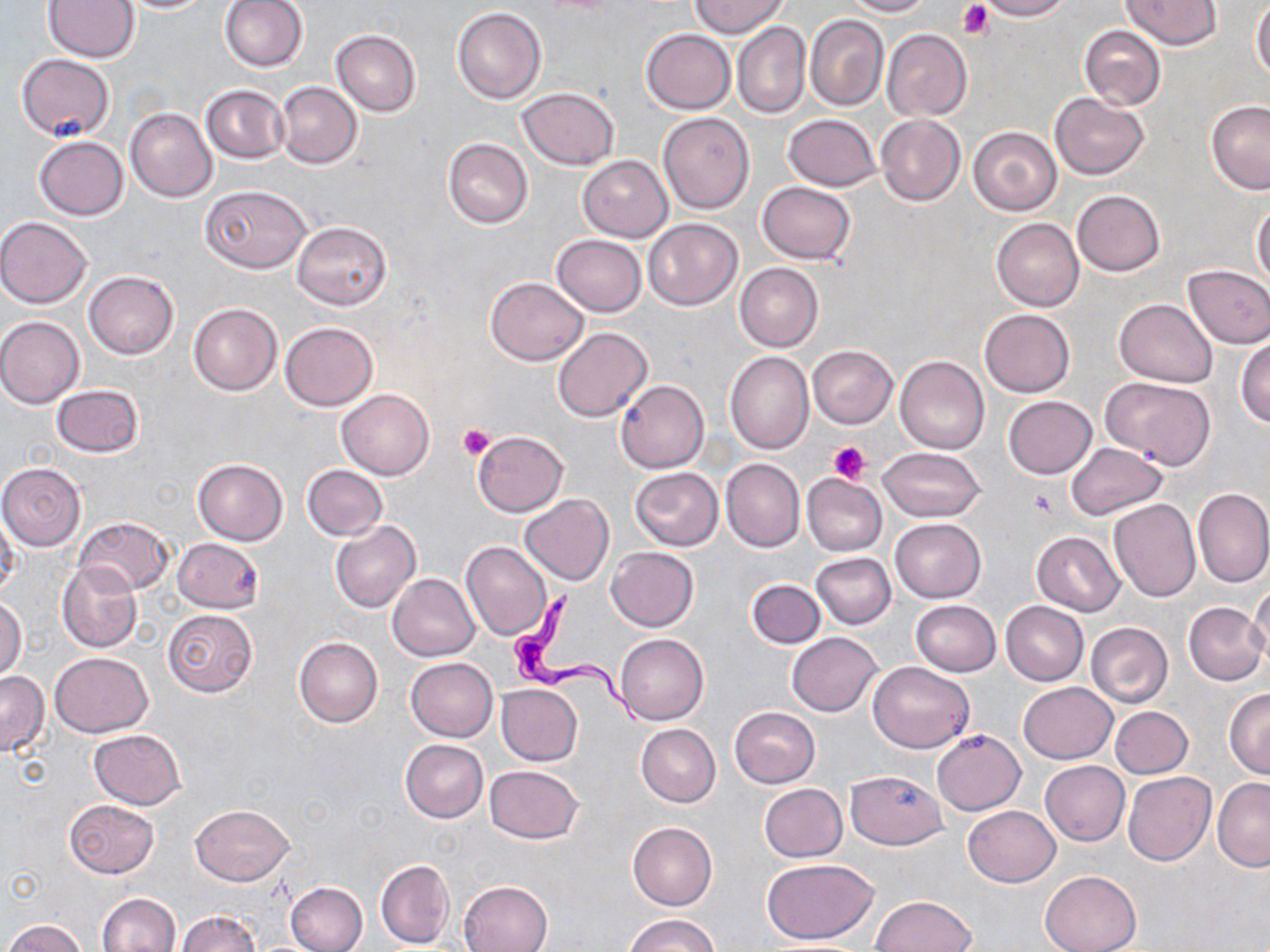

{
  "trypanosoma_brucei_locations": "approximate bounding boxes as named x1/y1/x2/y2 corners in pixels: (x1=506, y1=591, x2=645, y2=728)",
  "slide_level_diagnosis": "Trypanosoma brucei",
  "preparation": "thin blood film",
  "image_size": "1270×952 pixels",
  "platelet_locations": "approximate bounding boxes as named x1/y1/x2/y2 corners in pixels: (x1=958, y1=0, x2=994, y2=39), (x1=457, y1=424, x2=495, y2=459), (x1=829, y1=442, x2=870, y2=484), (x1=1028, y1=487, x2=1059, y2=517)",
  "magnification": "1000x",
  "stain": "May-Grünwald-Giemsa",
  "uninfected_red_blood_cell_locations": "approximate bounding boxes as named x1/y1/x2/y2 corners in pixels: (x1=219, y1=0, x2=308, y2=73), (x1=844, y1=0, x2=933, y2=16), (x1=974, y1=0, x2=1073, y2=21), (x1=1121, y1=0, x2=1219, y2=49), (x1=117, y1=1, x2=216, y2=13), (x1=691, y1=1, x2=785, y2=38), (x1=44, y1=2, x2=138, y2=62), (x1=1251, y1=2, x2=1270, y2=81), (x1=452, y1=7, x2=547, y2=105), (x1=804, y1=15, x2=889, y2=111), (x1=733, y1=22, x2=811, y2=119), (x1=1078, y1=25, x2=1166, y2=110), (x1=641, y1=28, x2=735, y2=114), (x1=330, y1=29, x2=421, y2=116), (x1=882, y1=29, x2=971, y2=120), (x1=18, y1=54, x2=115, y2=140), (x1=275, y1=82, x2=361, y2=168), (x1=201, y1=85, x2=289, y2=162), (x1=517, y1=87, x2=619, y2=170), (x1=1050, y1=92, x2=1149, y2=179), (x1=1206, y1=101, x2=1270, y2=195), (x1=124, y1=108, x2=217, y2=201), (x1=658, y1=112, x2=754, y2=214), (x1=783, y1=114, x2=881, y2=191), (x1=875, y1=114, x2=966, y2=207), (x1=968, y1=126, x2=1061, y2=216), (x1=34, y1=137, x2=129, y2=220), (x1=443, y1=138, x2=532, y2=228), (x1=578, y1=155, x2=673, y2=241), (x1=758, y1=181, x2=855, y2=263), (x1=200, y1=184, x2=311, y2=273), (x1=1072, y1=190, x2=1164, y2=276), (x1=1251, y1=201, x2=1270, y2=284), (x1=0, y1=217, x2=91, y2=308), (x1=644, y1=218, x2=742, y2=310), (x1=991, y1=218, x2=1084, y2=311), (x1=292, y1=221, x2=393, y2=310), (x1=550, y1=234, x2=646, y2=316), (x1=735, y1=263, x2=824, y2=351), (x1=1182, y1=263, x2=1270, y2=349), (x1=85, y1=271, x2=179, y2=358), (x1=484, y1=276, x2=589, y2=365), (x1=1115, y1=298, x2=1217, y2=387), (x1=188, y1=303, x2=281, y2=395), (x1=979, y1=309, x2=1075, y2=397), (x1=0, y1=316, x2=85, y2=408), (x1=279, y1=322, x2=378, y2=411), (x1=552, y1=328, x2=652, y2=422), (x1=1235, y1=338, x2=1270, y2=430), (x1=808, y1=345, x2=897, y2=428), (x1=725, y1=352, x2=813, y2=453), (x1=895, y1=356, x2=989, y2=454), (x1=1101, y1=376, x2=1216, y2=468), (x1=616, y1=379, x2=710, y2=473), (x1=51, y1=384, x2=144, y2=457), (x1=337, y1=389, x2=434, y2=480), (x1=1003, y1=396, x2=1096, y2=479), (x1=472, y1=431, x2=568, y2=516), (x1=1066, y1=442, x2=1168, y2=520), (x1=877, y1=447, x2=985, y2=523), (x1=721, y1=458, x2=805, y2=551), (x1=193, y1=459, x2=289, y2=545), (x1=0, y1=464, x2=87, y2=549), (x1=301, y1=465, x2=388, y2=541), (x1=629, y1=467, x2=724, y2=551), (x1=803, y1=472, x2=888, y2=557), (x1=1192, y1=488, x2=1270, y2=588), (x1=520, y1=495, x2=614, y2=585), (x1=1108, y1=500, x2=1201, y2=602), (x1=1, y1=510, x2=19, y2=599), (x1=75, y1=516, x2=175, y2=596), (x1=889, y1=518, x2=986, y2=602), (x1=330, y1=520, x2=421, y2=613), (x1=1031, y1=531, x2=1124, y2=617), (x1=171, y1=538, x2=264, y2=611), (x1=461, y1=541, x2=553, y2=641), (x1=606, y1=548, x2=698, y2=631), (x1=810, y1=553, x2=896, y2=629), (x1=57, y1=561, x2=141, y2=654), (x1=386, y1=573, x2=479, y2=661), (x1=746, y1=579, x2=826, y2=648), (x1=1248, y1=582, x2=1270, y2=666), (x1=0, y1=597, x2=25, y2=682), (x1=910, y1=600, x2=1001, y2=677), (x1=1000, y1=601, x2=1088, y2=685), (x1=1183, y1=601, x2=1267, y2=685), (x1=163, y1=609, x2=257, y2=697), (x1=1085, y1=622, x2=1173, y2=707), (x1=786, y1=631, x2=881, y2=717), (x1=615, y1=634, x2=709, y2=725), (x1=294, y1=635, x2=383, y2=727), (x1=50, y1=652, x2=152, y2=736), (x1=405, y1=658, x2=498, y2=742), (x1=867, y1=661, x2=975, y2=754), (x1=0, y1=671, x2=49, y2=757), (x1=1018, y1=682, x2=1118, y2=764), (x1=496, y1=684, x2=582, y2=766), (x1=1224, y1=689, x2=1270, y2=778), (x1=729, y1=706, x2=820, y2=789), (x1=1109, y1=706, x2=1193, y2=779), (x1=636, y1=724, x2=720, y2=807), (x1=88, y1=728, x2=186, y2=809), (x1=932, y1=730, x2=1025, y2=815), (x1=400, y1=740, x2=488, y2=823), (x1=1040, y1=760, x2=1130, y2=846), (x1=485, y1=765, x2=582, y2=844), (x1=845, y1=770, x2=945, y2=849), (x1=1122, y1=771, x2=1215, y2=866), (x1=1211, y1=778, x2=1270, y2=871), (x1=759, y1=783, x2=847, y2=861), (x1=64, y1=799, x2=159, y2=879), (x1=189, y1=804, x2=293, y2=885), (x1=963, y1=805, x2=1059, y2=887), (x1=627, y1=821, x2=717, y2=911), (x1=762, y1=858, x2=881, y2=943), (x1=376, y1=860, x2=455, y2=948), (x1=1040, y1=870, x2=1140, y2=952), (x1=285, y1=880, x2=367, y2=952), (x1=457, y1=881, x2=551, y2=951), (x1=97, y1=892, x2=179, y2=952), (x1=869, y1=895, x2=976, y2=952), (x1=176, y1=911, x2=260, y2=952), (x1=623, y1=913, x2=720, y2=952), (x1=2, y1=918, x2=87, y2=952)",
  "modality": "optical microscopy",
  "field_of_view": "one of a larger specimen"
}